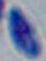

modality: photomicrograph
magnification: 1000x
identification: Toxoplasma gondii